Assess this cell for malaria.
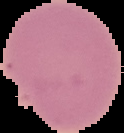
It is uninfected.

{
  "image_type": "segmented cell region on a black background",
  "preparation": "thin blood smear",
  "image_size": "124×133 pixels"
}